Describe the morphology of the red blood cells.
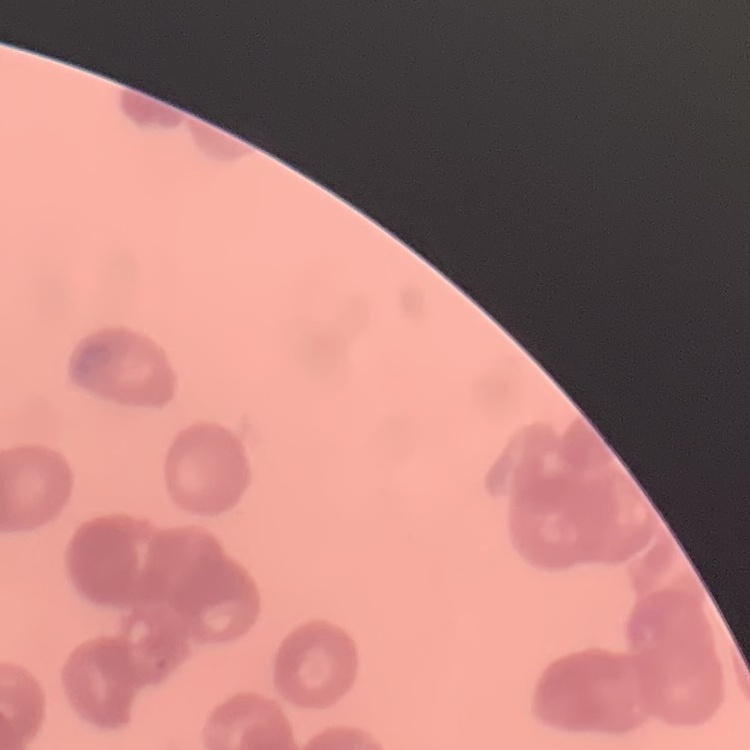

They show rouleaux formation.

preparation = thin peripheral smear
image type = square crop of a larger photomicrograph
stain = Field's or Giemsa